Identify the parasite.
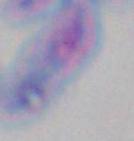
Toxoplasma gondii.

magnification = 1000x
modality = photomicrograph